Classify this cell by malaria status.
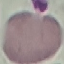
Uninfected.

Thin blood film. Photographed with a smartphone camera at the microscope eyepiece. Automatically extracted cell patch, resized to 64 × 64 pixels. Giemsa-stained preparation.